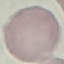
malaria_status: uninfected
image_type: automatically extracted cell patch, resized to 64 × 64 pixels
stain: Giemsa
capture: smartphone through the microscope eyepiece
preparation: thin smear